Locate every blood parasite and identify its species.
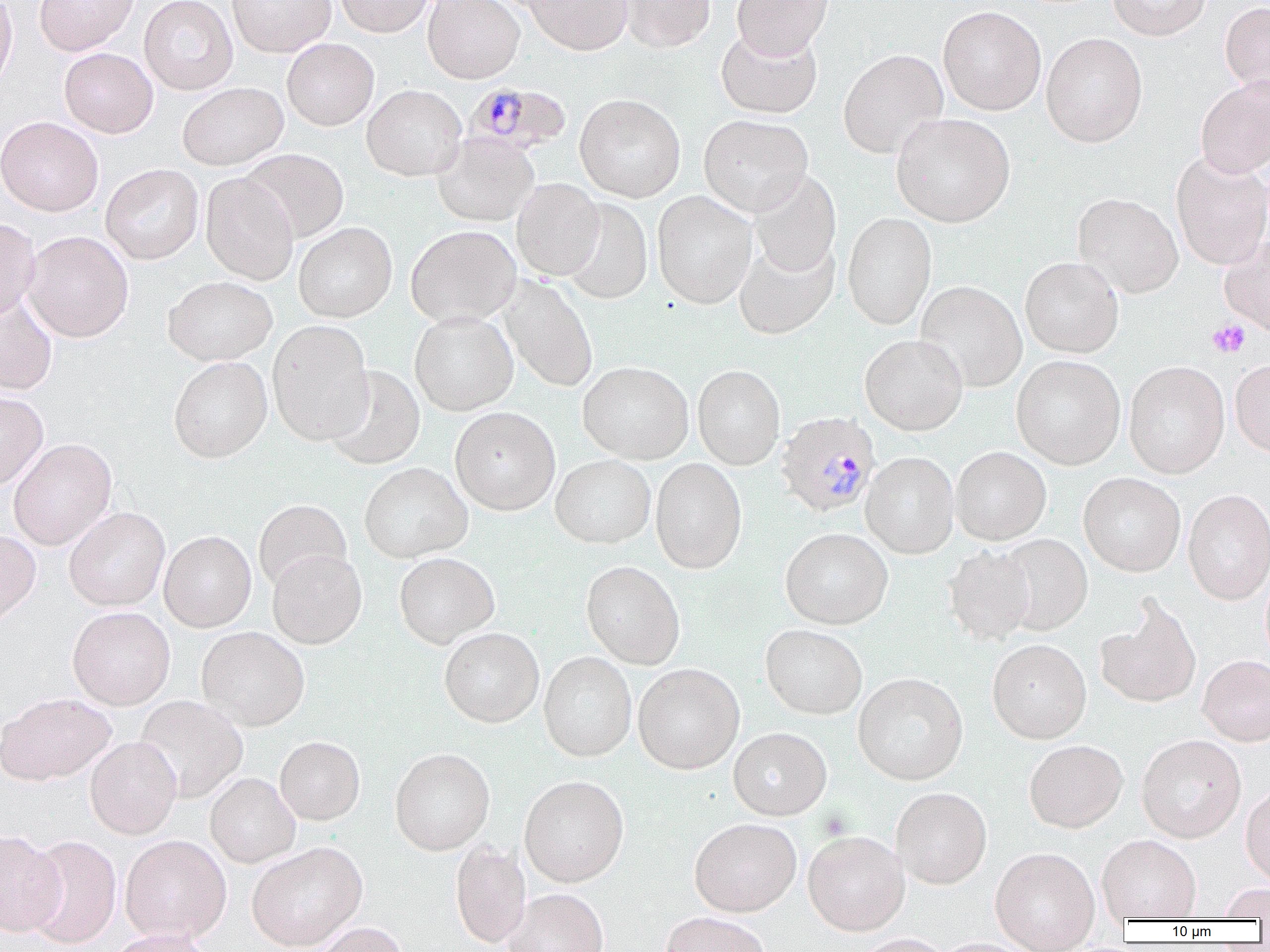

Approximate bounding boxes as [x1, y1, x2, y2] in pixels.
Plasmodium malariae-infected red blood cells: [469, 84, 576, 157], [776, 411, 880, 518].
No Plasmodium falciparum, Plasmodium ovale, Plasmodium vivax, Babesia divergens, or Trypanosoma brucei observed.

slide-level diagnosis = Plasmodium malariae
image size = 1270×952 pixels
uninfected red blood cell locations = approximate bounding boxes as [x1, y1, x2, y2] in pixels: [0, 0, 17, 90], [34, 0, 139, 56], [139, 0, 238, 95], [227, 0, 336, 57], [335, 0, 435, 37], [422, 0, 525, 84], [524, 0, 633, 55], [619, 0, 715, 53], [732, 0, 833, 58], [1107, 0, 1211, 41], [1220, 1, 1270, 100], [938, 5, 1046, 116], [715, 25, 823, 119], [1041, 32, 1147, 147], [282, 38, 379, 131], [59, 48, 157, 138], [838, 48, 948, 159], [1195, 77, 1270, 179], [177, 82, 288, 170], [362, 84, 467, 181], [575, 93, 686, 202], [890, 112, 1015, 227], [699, 114, 813, 217], [0, 116, 103, 216], [432, 133, 539, 226], [240, 148, 349, 243], [1170, 152, 1270, 271], [100, 164, 204, 264], [749, 170, 841, 277], [200, 173, 298, 285], [512, 178, 605, 280], [652, 191, 757, 309], [1072, 193, 1183, 298], [559, 198, 653, 305], [842, 212, 937, 330], [0, 217, 40, 320], [293, 222, 397, 323], [405, 225, 521, 327], [22, 231, 134, 342], [1219, 236, 1270, 338], [733, 237, 840, 339], [1020, 257, 1123, 358], [163, 275, 277, 366], [498, 275, 598, 393], [915, 281, 1027, 393], [0, 290, 58, 396], [409, 311, 519, 415], [267, 320, 374, 446], [859, 334, 968, 435], [1011, 355, 1125, 469], [168, 357, 272, 463], [1230, 358, 1270, 458], [578, 361, 694, 464], [1123, 361, 1230, 478], [693, 364, 785, 470], [323, 366, 425, 470], [0, 391, 48, 490], [450, 407, 561, 515], [8, 438, 117, 551], [951, 447, 1051, 545], [860, 451, 960, 559], [550, 455, 655, 549], [650, 458, 747, 574], [359, 462, 472, 563], [1079, 473, 1185, 577], [1183, 489, 1270, 604], [253, 500, 352, 593], [63, 507, 170, 611], [780, 527, 893, 629], [0, 529, 41, 628], [159, 530, 257, 632], [998, 534, 1093, 634], [943, 546, 1037, 644], [267, 549, 367, 649], [394, 552, 500, 648], [581, 560, 685, 670], [1095, 597, 1202, 708], [67, 607, 175, 710], [760, 624, 868, 720], [197, 627, 309, 731], [439, 628, 544, 727], [987, 640, 1092, 743], [539, 651, 637, 762], [1197, 655, 1270, 746], [633, 663, 745, 774], [853, 673, 968, 784], [0, 692, 116, 785], [134, 695, 248, 803], [728, 727, 832, 820], [275, 735, 365, 825], [1136, 735, 1246, 842], [85, 736, 181, 839], [1024, 740, 1128, 833], [390, 748, 494, 855], [205, 772, 301, 868], [519, 775, 629, 887], [1240, 783, 1270, 887], [891, 788, 992, 889], [689, 818, 802, 916], [0, 829, 66, 937], [803, 831, 910, 935], [120, 834, 231, 943], [1097, 834, 1201, 922], [25, 835, 122, 948], [246, 841, 368, 951], [450, 841, 532, 949], [990, 847, 1100, 950], [1215, 883, 1270, 919], [504, 888, 609, 952], [660, 911, 771, 952], [311, 921, 409, 952], [106, 928, 214, 952], [850, 934, 954, 952], [928, 937, 1042, 952]
field of view = single
modality = optical microscopy
magnification = 1000x
preparation = thin blood smear
platelet locations = approximate bounding boxes as [x1, y1, x2, y2] in pixels: [1208, 319, 1251, 358]